Comment on the morphology of the red blood cells.
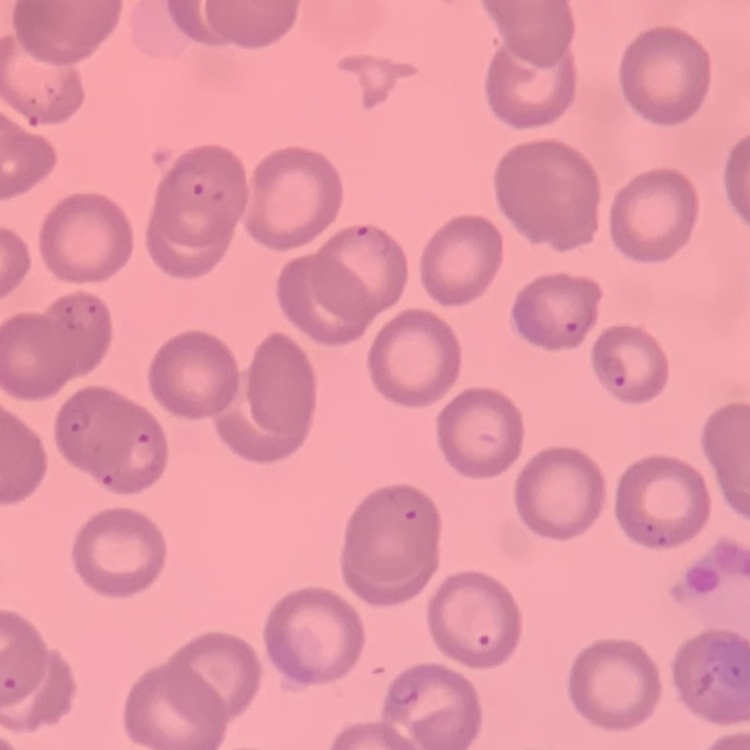
No rouleaux formation.

Summary:
  - Stain: Field's or Giemsa
  - Image type: one tile cut from a larger photomicrograph
  - Preparation: thin peripheral smear